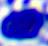

Summary:
  - Modality: micrograph
  - Identification: white blood cell
  - Magnification: 400x